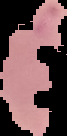

image_type: segmented cell region with the area outside set to black
image_size: 67×136 pixels
result: Plasmodium parasites detected
preparation: thin blood smear